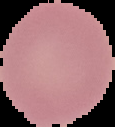
Summary:
  - Preparation: thin blood film
  - Image size: 115×127 pixels
  - Result: no malaria parasites seen
  - Image type: segmented cell region with the area outside set to black